Comment on the morphology of the red blood cells.
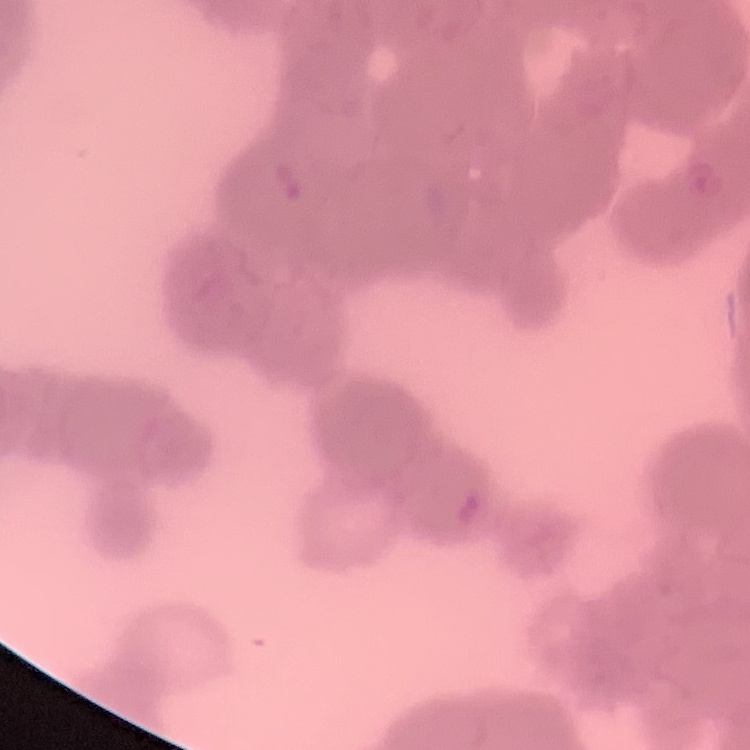

Rouleaux formation.

One tile cut from a larger photomicrograph. Thin peripheral smear. Field's or Giemsa stain.